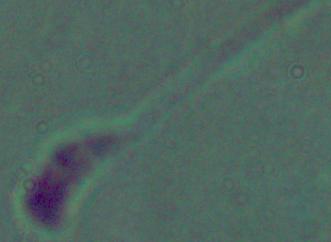

Summary:
  - Modality: micrograph
  - Magnification: 1000x
  - Identification: Leishmania